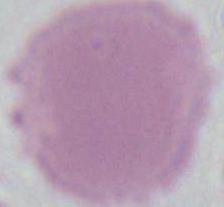

Summary:
  - Identification: red blood cell
  - Magnification: 1000x
  - Modality: photomicrograph